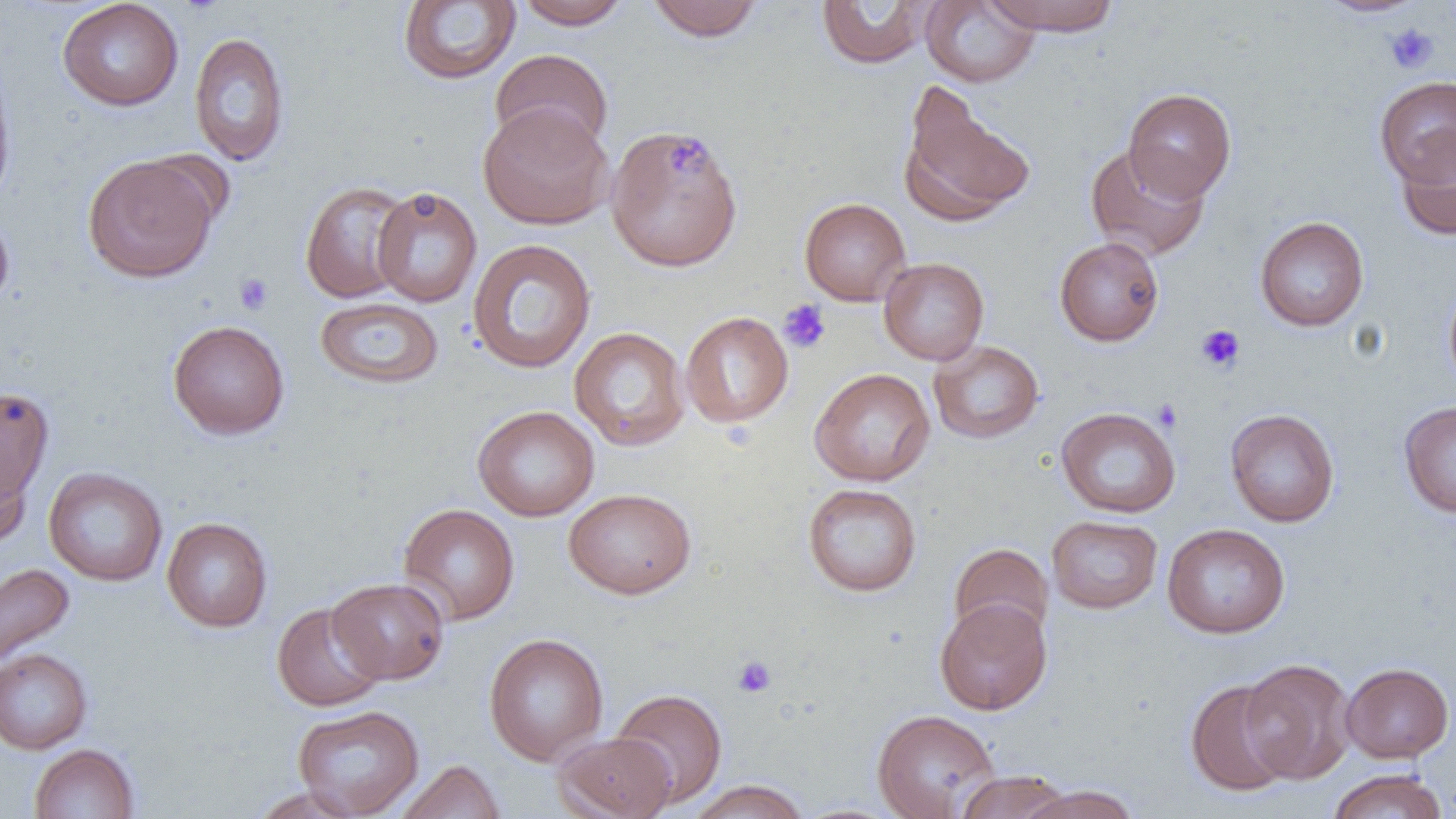

slide-level diagnosis = no evidence of blood parasites
preparation = thin blood film
modality = optical microscopy
uninfected red blood cell locations = approximate bounding boxes as [x1, y1, x2, y2] in pixels: [57, 0, 184, 111], [514, 0, 632, 30], [646, 0, 764, 42], [816, 0, 938, 69], [920, 0, 1040, 87], [983, 0, 1122, 35], [1316, 0, 1427, 17], [399, 1, 521, 84], [189, 31, 290, 167], [490, 48, 614, 154], [0, 56, 17, 212], [1375, 76, 1456, 186], [899, 83, 1036, 227], [1123, 88, 1237, 202], [478, 103, 614, 230], [606, 125, 743, 272], [1396, 132, 1456, 242], [1085, 144, 1210, 261], [83, 154, 220, 283], [300, 180, 415, 303], [371, 186, 482, 307], [799, 197, 911, 306], [0, 204, 15, 313], [1255, 216, 1369, 331], [1054, 236, 1164, 346], [467, 239, 596, 373], [878, 257, 990, 365], [1443, 278, 1456, 394], [315, 296, 444, 388], [680, 311, 793, 428], [167, 319, 290, 440], [568, 326, 691, 451], [928, 339, 1044, 444], [810, 367, 935, 486], [0, 385, 55, 508], [1398, 400, 1456, 517], [472, 405, 599, 521], [1055, 406, 1181, 518], [1225, 408, 1340, 527], [0, 447, 32, 548], [43, 467, 167, 586], [802, 483, 922, 597], [563, 488, 696, 599], [398, 503, 520, 625], [1047, 515, 1163, 614], [162, 517, 273, 633], [1162, 523, 1290, 638], [949, 543, 1053, 644], [0, 562, 75, 669], [328, 577, 450, 684], [934, 598, 1052, 715], [272, 601, 387, 711], [484, 632, 609, 766], [0, 648, 92, 754], [1240, 658, 1356, 783], [1340, 662, 1454, 763], [1184, 679, 1295, 797], [610, 688, 728, 808], [292, 704, 424, 818], [872, 708, 1001, 818], [552, 732, 676, 819], [29, 743, 140, 819], [395, 759, 506, 819], [1327, 768, 1448, 819], [953, 770, 1074, 818], [686, 780, 812, 819], [1019, 784, 1140, 819], [250, 786, 365, 818]
magnification = 1000x
field of view = one of a larger specimen
image size = 1456×819 pixels
platelet locations = approximate bounding boxes as [x1, y1, x2, y2] in pixels: [1384, 22, 1439, 73], [234, 273, 274, 315], [778, 299, 831, 354], [1195, 324, 1245, 373], [1152, 398, 1183, 432], [732, 656, 776, 698]